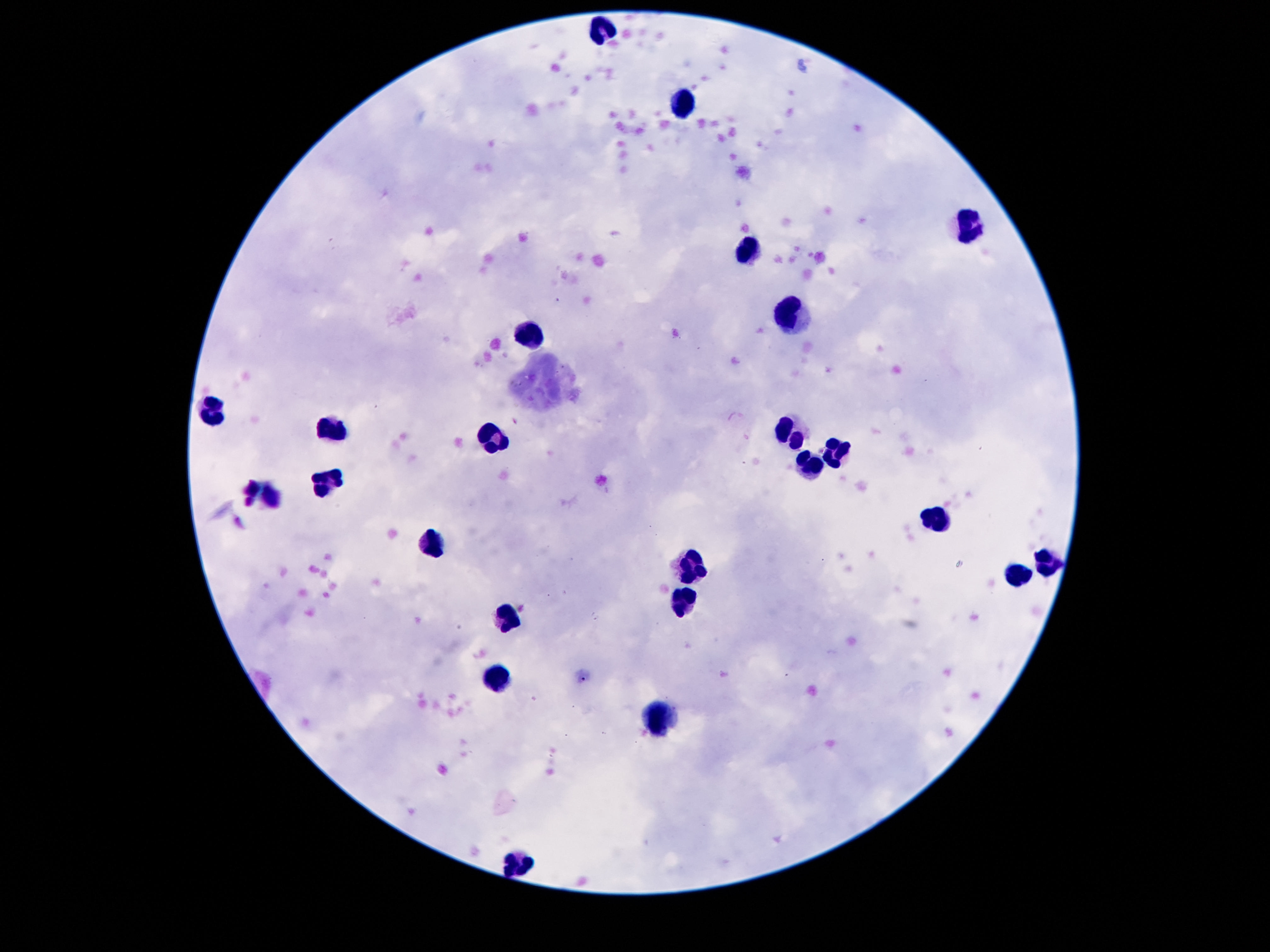 Approximate centers as (x, y) in pixels. Leukocyte locations: (598, 29), (680, 104), (964, 227), (748, 251), (791, 313), (536, 333), (215, 411), (331, 429), (790, 432), (835, 449), (808, 466), (329, 481), (932, 518), (430, 545), (1045, 562), (690, 567), (1018, 577), (684, 602), (511, 626), (497, 679), (652, 716), (516, 861). Smartphone photograph taken through the microscope eyepiece. Giemsa-stained preparation. Patient malaria status: not infected. 100x magnification. Image is 1270×952 pixels. Thick blood film. Single field of view.